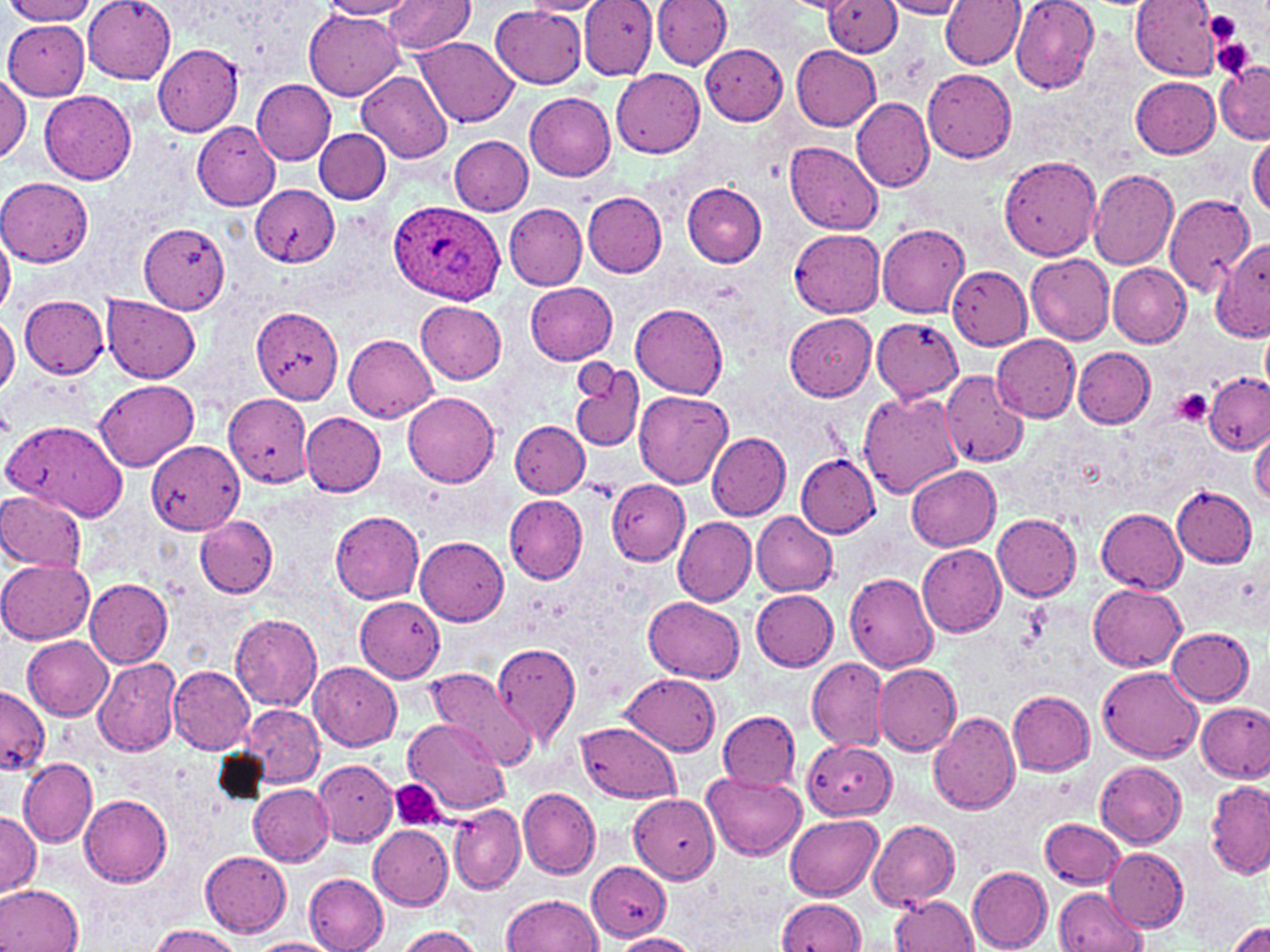

Approximate bounding boxes as (x1,y1)-(x2,y2) corner pairs in pixels. Uninfected red blood cell locations: (6,0)-(99,24), (84,0)-(176,82), (324,0)-(416,19), (385,0)-(476,53), (579,0)-(659,79), (653,0)-(733,72), (1010,0)-(1099,93), (1131,0)-(1222,79), (519,1)-(609,15), (825,1)-(902,56), (881,1)-(970,19), (938,2)-(1023,69), (490,8)-(590,88), (305,10)-(404,99), (3,20)-(89,99), (416,37)-(519,128), (700,42)-(788,125), (153,45)-(244,135), (792,46)-(880,130), (1217,60)-(1269,144), (611,69)-(705,158), (923,69)-(1017,163), (358,71)-(453,163), (0,74)-(30,163), (1132,76)-(1220,159), (252,79)-(335,165), (41,90)-(136,184), (524,92)-(616,180), (852,98)-(935,192), (191,120)-(280,210), (314,128)-(391,203), (448,136)-(532,215), (1247,137)-(1269,216), (785,141)-(883,233), (1000,155)-(1103,260), (1087,166)-(1179,269), (1,178)-(92,265), (683,183)-(767,267), (250,186)-(338,267), (582,191)-(667,278), (1162,194)-(1255,296), (505,203)-(588,290), (139,221)-(229,313), (877,223)-(969,318), (0,229)-(15,316), (789,229)-(885,317), (1212,243)-(1270,341), (1025,252)-(1115,345), (1107,263)-(1191,347), (947,266)-(1032,350), (525,282)-(618,365), (101,295)-(201,383), (20,296)-(109,379), (415,301)-(507,384), (630,304)-(728,397), (252,306)-(344,403), (785,314)-(877,401), (0,317)-(19,396), (872,318)-(963,402), (1261,326)-(1270,393), (343,332)-(437,421), (992,333)-(1083,421), (1073,347)-(1155,427), (570,360)-(645,453), (940,370)-(1027,467), (1203,371)-(1269,455), (95,379)-(200,471), (635,390)-(734,488), (858,390)-(964,498), (403,391)-(499,486), (225,393)-(311,485), (300,412)-(386,495), (2,418)-(129,523), (509,419)-(590,497), (1250,424)-(1270,508), (707,432)-(790,519), (146,440)-(245,534), (796,455)-(878,537), (906,465)-(1001,551), (608,478)-(689,566), (1171,486)-(1258,568), (0,490)-(87,573), (504,495)-(587,584), (1095,508)-(1187,593), (751,510)-(837,595), (331,511)-(424,603), (992,514)-(1082,601), (194,516)-(277,598), (674,517)-(755,606), (416,537)-(509,626), (917,544)-(1006,638), (0,560)-(94,643), (845,573)-(940,672), (85,579)-(173,668), (1089,584)-(1186,671), (751,589)-(838,670), (353,597)-(444,682), (645,597)-(744,681), (230,611)-(323,711), (1166,627)-(1256,705), (23,636)-(113,720), (491,642)-(580,748), (92,657)-(182,757), (807,657)-(888,752), (309,662)-(402,750), (873,662)-(961,756), (1097,664)-(1204,762), (168,665)-(256,754), (425,665)-(537,770), (623,672)-(722,756), (0,687)-(50,774), (1008,691)-(1096,774), (1198,701)-(1270,781), (241,705)-(324,787), (717,711)-(801,792), (928,711)-(1020,816), (403,717)-(507,816), (576,722)-(682,802), (804,739)-(895,820), (20,758)-(97,846), (315,759)-(398,848), (1094,760)-(1187,847), (703,772)-(806,861), (1205,781)-(1270,878), (248,782)-(334,866), (519,788)-(600,878), (630,792)-(720,883), (80,794)-(173,887), (450,802)-(526,894), (0,811)-(42,898), (784,813)-(884,899), (1042,817)-(1125,889), (869,820)-(960,908), (368,826)-(452,909), (1105,848)-(1188,930), (200,852)-(292,936), (586,861)-(671,939), (967,868)-(1053,951), (303,873)-(388,951), (0,884)-(83,952), (1055,887)-(1147,952), (500,895)-(603,952), (889,895)-(978,952), (776,899)-(866,952), (1230,921)-(1270,952), (147,925)-(241,952), (394,926)-(484,952), (608,933)-(700,952), (250,938)-(339,952). Platelet locations: (1204,9)-(1245,44), (1210,36)-(1257,80), (1173,389)-(1213,426), (389,780)-(448,832). Plasmodium ovale-infected red blood cell locations: (387,200)-(507,304). Slide-level diagnosis: Plasmodium ovale. 1000x magnification. Single field of view. Image is 1270×952 pixels. Optical microscopy. May-Grünwald-Giemsa stain. Thin blood smear.